State which parasite is depicted.
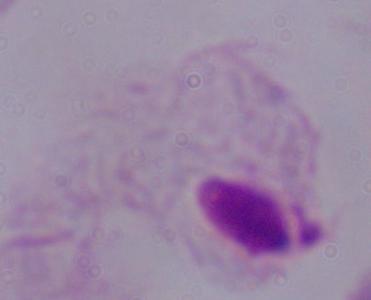
A trichomonad.

Summary:
  - Modality: micrograph
  - Magnification: 1000x